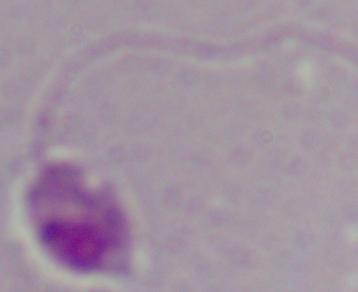
Summary:
  - Identification: Leishmania
  - Modality: micrograph
  - Magnification: 1000x